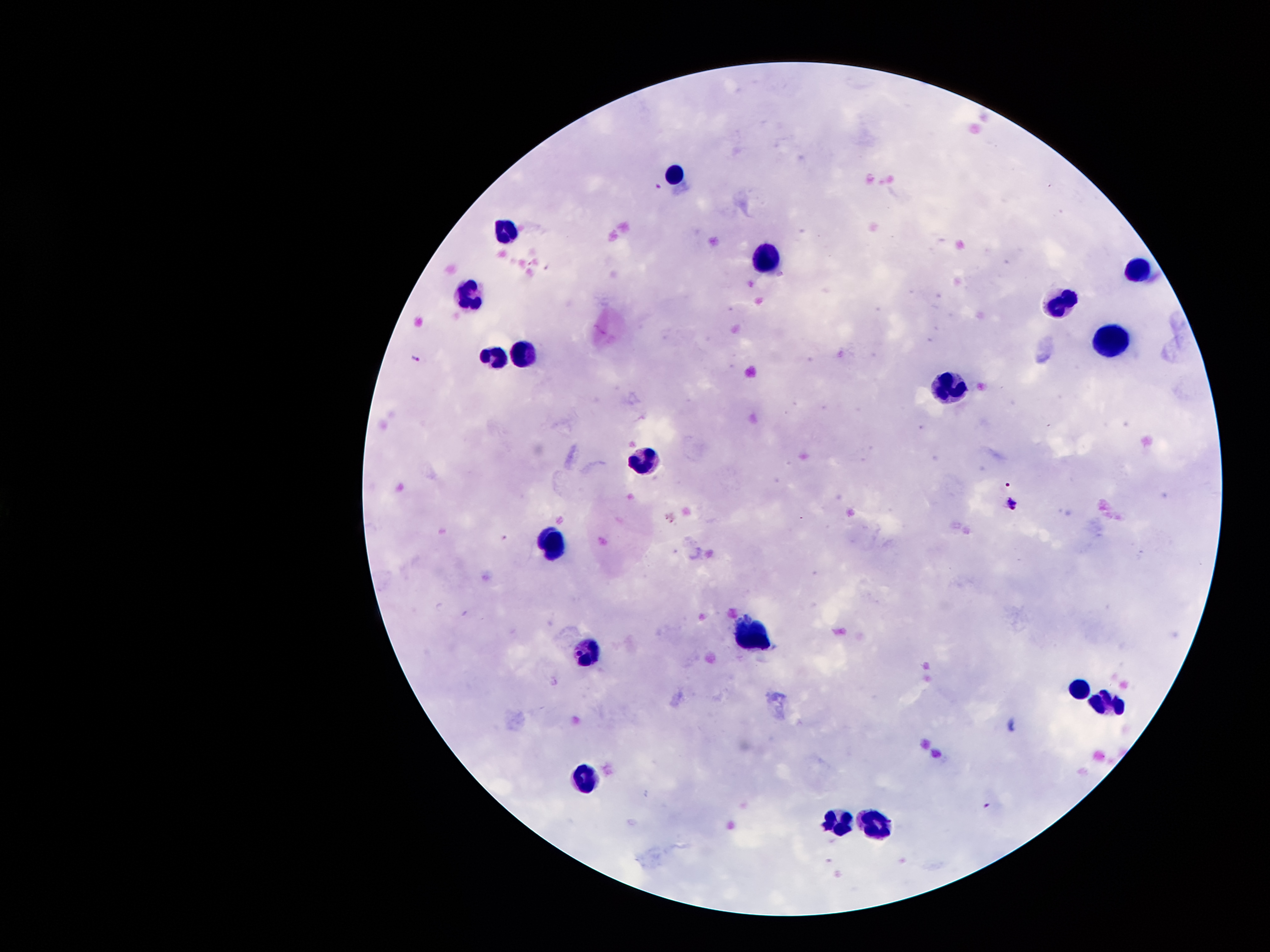
Approximate centers as [x, y] in pixels.
Summary:
  - Leukocyte locations: [672, 168], [504, 227], [767, 248], [1137, 267], [466, 293], [1060, 300], [1111, 335], [524, 349], [493, 353], [948, 382], [643, 463], [552, 544], [748, 635], [590, 652], [1077, 687], [1109, 701], [584, 780], [837, 819], [874, 822]
  - Malaria parasite locations: [660, 187], [414, 359], [1009, 485], [1012, 504], [987, 805]
  - Preparation: thick blood smear
  - Stain: Giemsa
  - Magnification: 100x
  - Field of view: one from this slide
  - Image size: 1270×952 pixels
  - Patient malaria status: infected with Plasmodium falciparum
  - Capture: smartphone through the microscope eyepiece